Identify the preparation type.
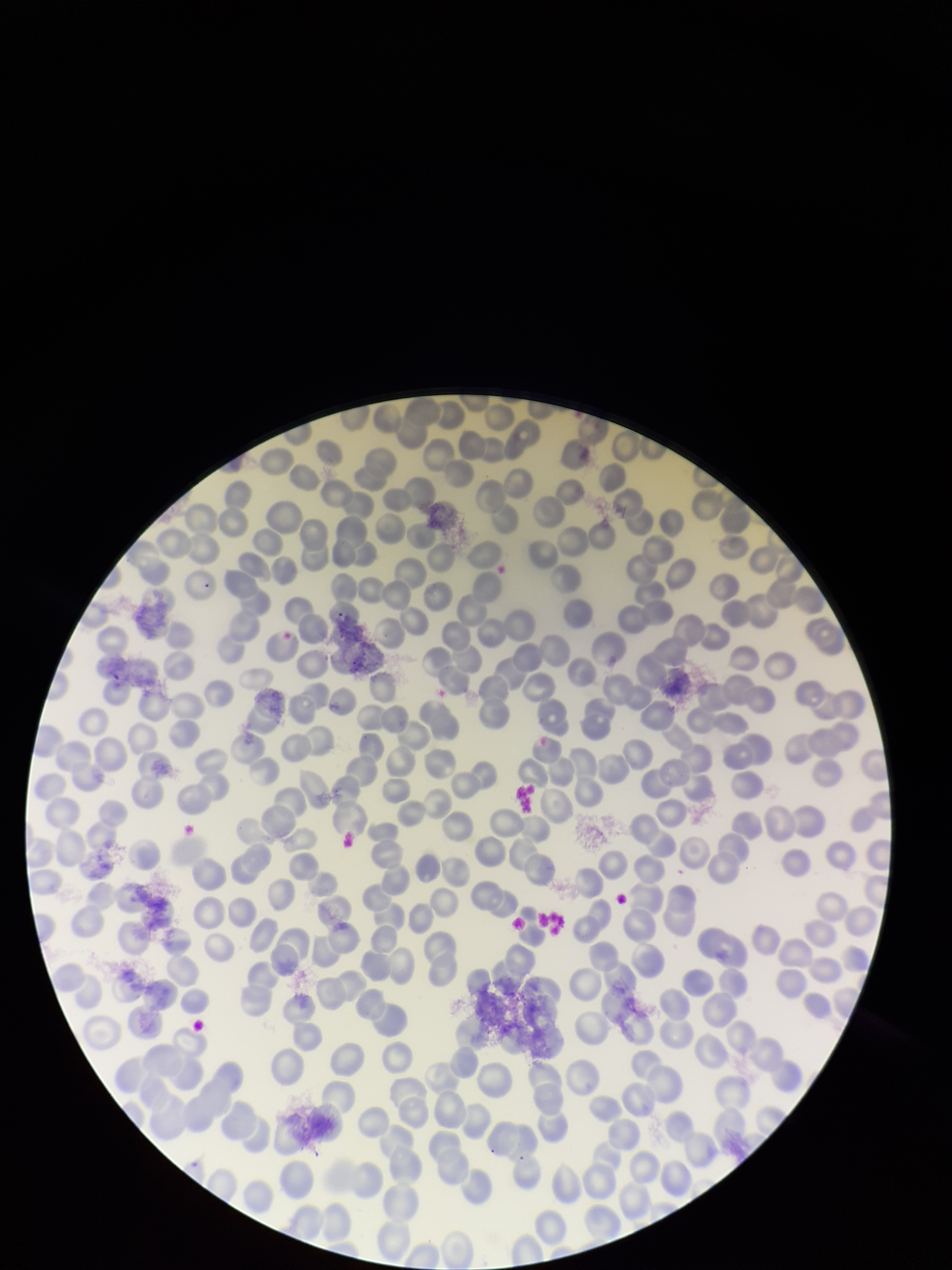

A thin smear.

Parasitized red blood cell count: 0. Patient malaria status: negative. Giemsa stain. Photographed through the microscope eyepiece with a smartphone camera. Image is 952×1270 pixels. Single field of view. Parasitized red blood cells: none identified. Red blood cell count: 229.